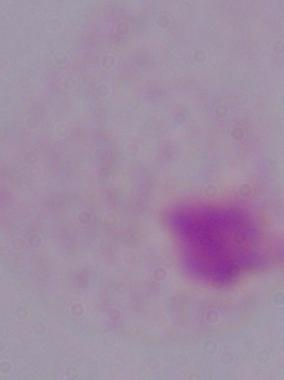

modality = micrograph
identification = trichomonad
magnification = 1000x